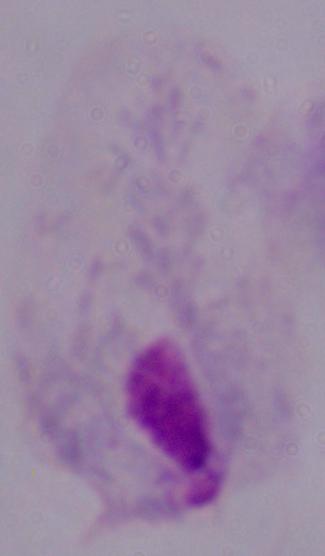
Summary:
  - Magnification: 1000x
  - Modality: micrograph
  - Identification: trichomonad